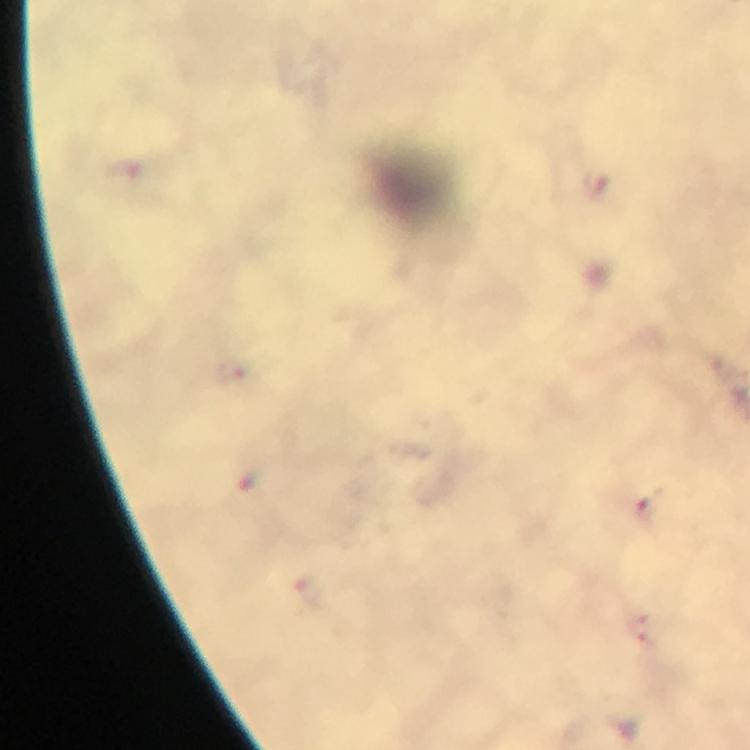
context = from a diagnostic examination for malaria
stain = Giemsa
magnification = 100x
image size = 750×750 pixels
preparation = thick blood film
immersion oil = used
Plasmodium parasite locations = approximate centers as (x, y) in pixels: (655, 510)
cropped from = a single field of view
capture = smartphone camera through the microscope